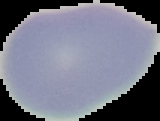
Segmented cell region on a black background. From a thin blood smear. Malaria status: uninfected. Image is 160×121 pixels.